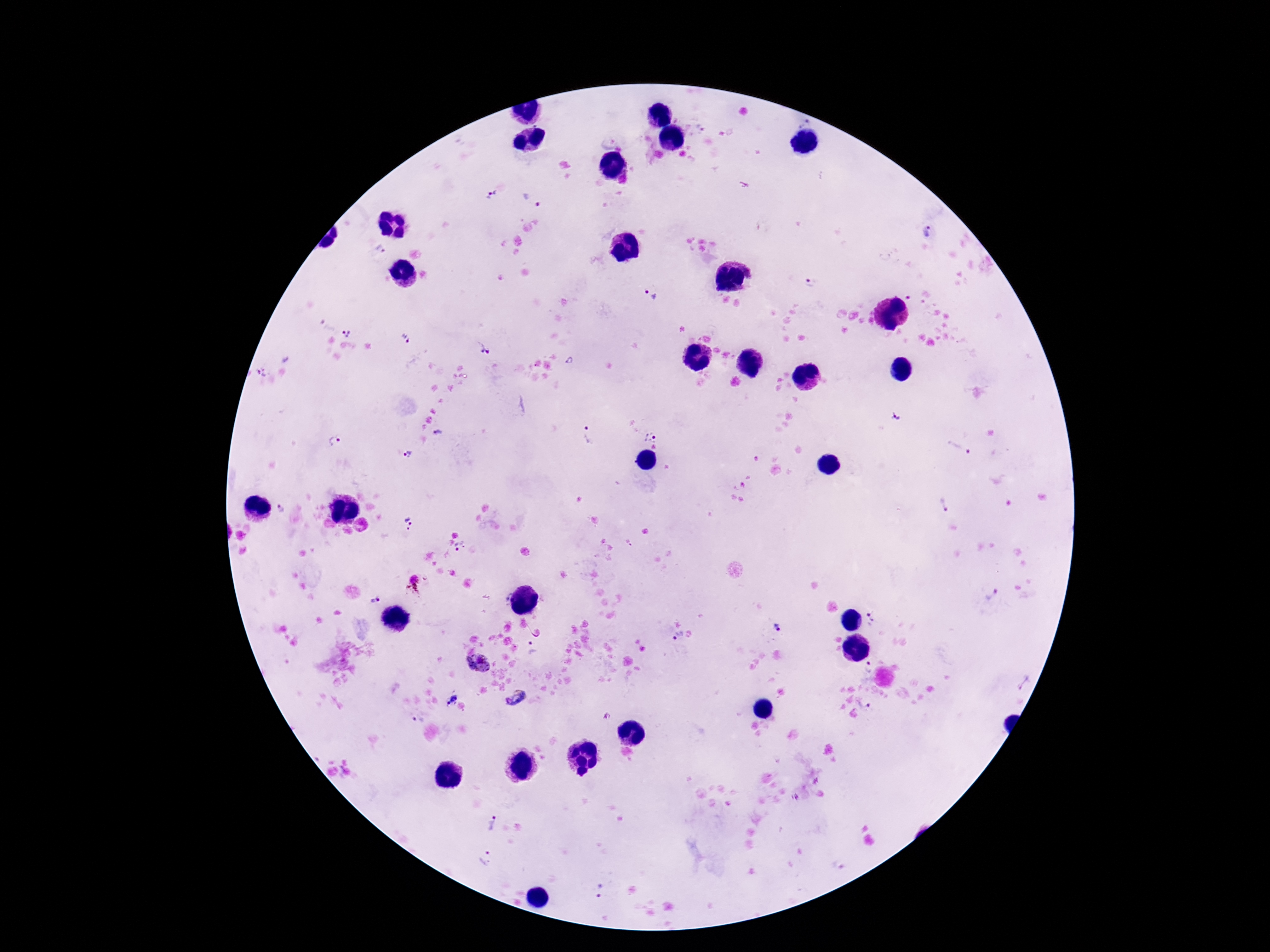
Approximate centers as (x, y) in pixels.
Summary:
  - Plasmodium parasite locations: (701, 126), (491, 195), (532, 199), (930, 232), (380, 250), (809, 283), (653, 295), (346, 332), (405, 338), (483, 348), (568, 361), (261, 373), (895, 417), (437, 434), (589, 435), (649, 437), (334, 440), (958, 448), (409, 454), (943, 505), (409, 521), (629, 544), (461, 547), (411, 586), (992, 595), (376, 600), (870, 619), (777, 628), (678, 637), (533, 648), (478, 664), (869, 667), (1024, 682), (518, 698), (451, 700), (865, 704), (417, 720), (491, 823), (485, 859), (838, 864), (600, 892)
  - Magnification: 100x
  - Capture: smartphone camera through the microscope eyepiece
  - Patient malaria status: infected
  - Image size: 1270×952 pixels
  - Field of view: one from this slide
  - Stain: Giemsa
  - Preparation: thick peripheral-blood smear